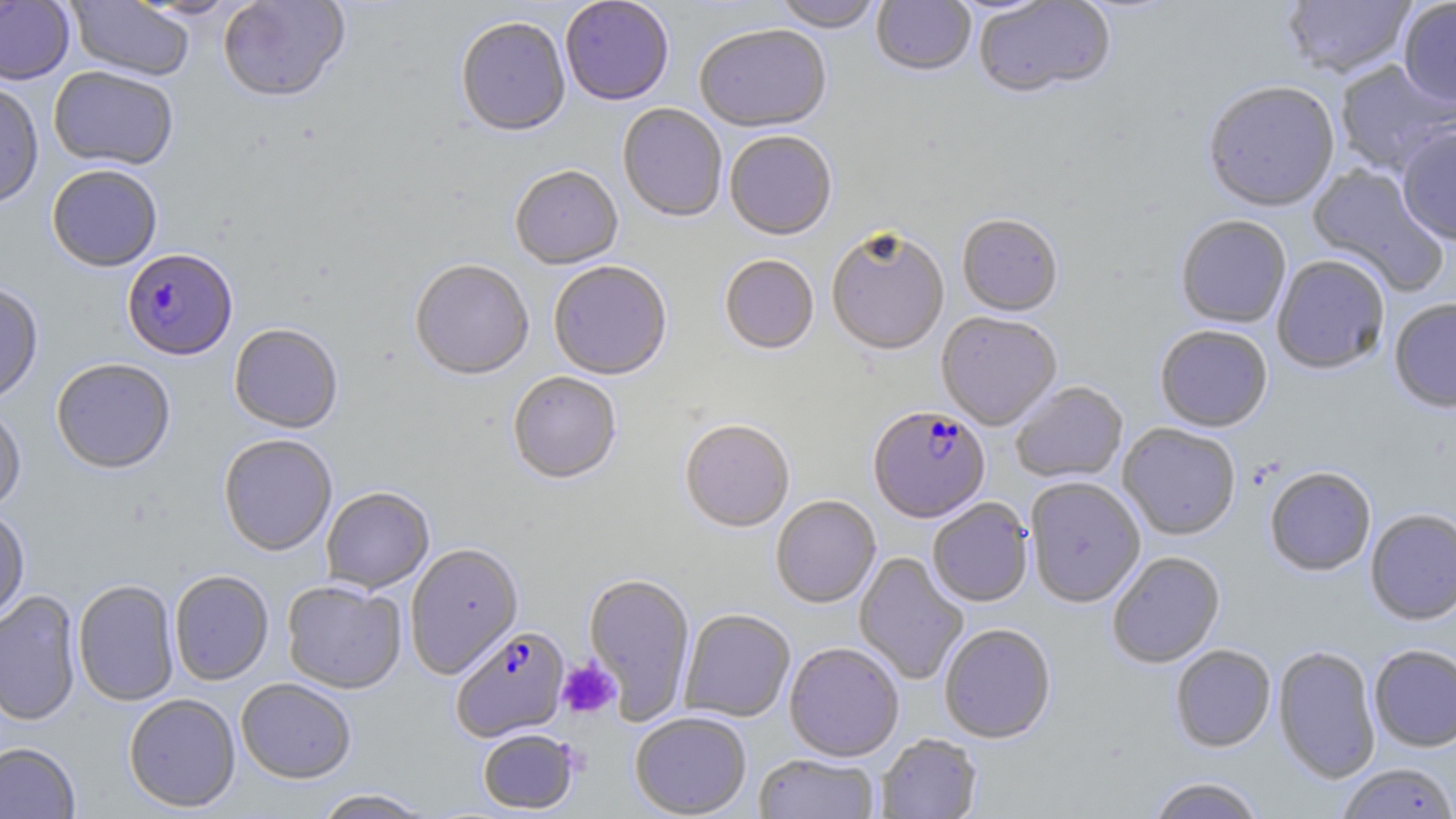
Approximate bounding boxes as (x1,y1)-(x2,y2) corner pairs in pixels. Platelet locations: (557,659)-(620,719). Uninfected red blood cell locations: (65,0)-(194,83), (217,0)-(351,105), (774,0)-(884,34), (974,0)-(1116,101), (1281,0)-(1417,82), (0,1)-(75,85), (125,1)-(248,21), (560,1)-(674,107), (871,1)-(976,79), (1397,1)-(1456,111), (456,18)-(571,139), (695,27)-(831,135), (1335,60)-(1455,176), (49,66)-(179,170), (0,81)-(44,209), (1203,83)-(1340,215), (617,104)-(727,224), (1396,127)-(1456,246), (725,133)-(837,242), (1306,164)-(1449,296), (47,165)-(163,272), (510,167)-(623,272), (957,216)-(1063,318), (1175,217)-(1291,329), (826,232)-(949,358), (719,256)-(819,356), (1272,256)-(1390,376), (410,261)-(534,381), (548,262)-(672,381), (0,282)-(44,406), (1389,299)-(1456,415), (937,313)-(1062,431), (229,324)-(343,434), (1155,326)-(1272,433), (51,359)-(175,474), (508,373)-(622,486), (1011,382)-(1128,484), (0,406)-(26,513), (680,421)-(795,534), (1118,425)-(1241,542), (218,435)-(337,557), (1264,468)-(1376,578), (1025,478)-(1145,608), (321,487)-(434,593), (771,496)-(881,609), (928,499)-(1033,607), (0,507)-(30,624), (1365,509)-(1456,625), (405,544)-(523,679), (854,552)-(969,686), (1107,552)-(1225,669), (169,570)-(274,686), (583,574)-(695,723), (73,579)-(180,706), (282,581)-(406,694), (0,591)-(82,726), (679,609)-(795,723), (939,625)-(1056,743), (784,643)-(904,762), (1369,644)-(1456,752), (1170,645)-(1276,753), (1273,646)-(1381,784), (236,678)-(356,784), (124,693)-(241,813), (630,712)-(751,818), (477,728)-(580,814), (875,734)-(982,818), (0,742)-(81,818), (754,754)-(880,819), (1336,764)-(1456,819), (1145,777)-(1267,819), (311,788)-(436,818). Plasmodium falciparum-infected red blood cell locations: (122,249)-(237,362), (868,408)-(991,524), (452,626)-(569,742). Slide-level diagnosis: Plasmodium falciparum. Image is 1456×819 pixels. 1000x magnification. One field of a larger specimen. Optical microscopy. May-Grünwald-Giemsa-stained preparation. Thin blood film.